State the blood parasite species.
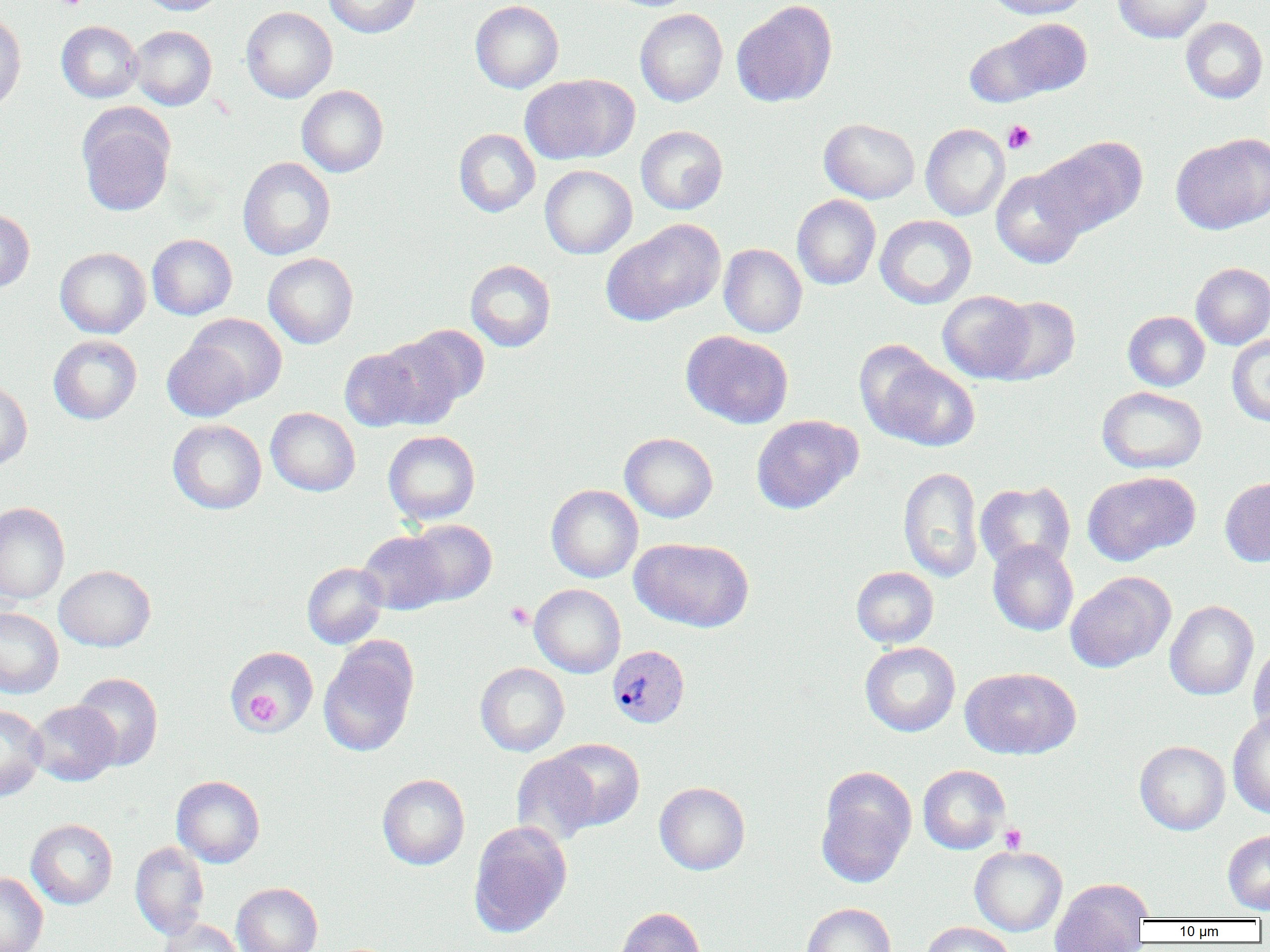
Plasmodium vivax.

Summary:
  - Coordinate format: approximate bounding boxes as [x1, y1, x2, y2] in pixels
  - Plasmodium vivax-infected red blood cell locations: [607, 644, 690, 729]
  - Platelet locations: [53, 0, 89, 11], [1002, 120, 1036, 154], [505, 602, 533, 629], [245, 691, 280, 728], [1000, 824, 1027, 853]
  - Uninfected red blood cell locations: [137, 0, 228, 16], [324, 0, 421, 38], [986, 0, 1089, 19], [1112, 0, 1213, 43], [470, 1, 564, 93], [731, 2, 837, 107], [240, 6, 338, 103], [635, 8, 728, 106], [0, 14, 26, 113], [997, 17, 1093, 98], [1181, 17, 1268, 104], [56, 21, 143, 103], [129, 25, 217, 110], [963, 30, 1056, 107], [520, 74, 637, 165], [297, 85, 389, 177], [77, 107, 175, 217], [819, 118, 920, 203], [921, 123, 1010, 221], [636, 125, 728, 214], [453, 128, 540, 217], [1170, 133, 1270, 234], [1036, 137, 1148, 236], [237, 157, 336, 260], [540, 165, 637, 259], [991, 168, 1086, 268], [792, 194, 881, 290], [0, 208, 34, 294], [875, 215, 977, 309], [602, 219, 725, 325], [147, 234, 237, 319], [719, 244, 807, 337], [55, 247, 151, 338], [263, 253, 358, 349], [465, 259, 556, 352], [1191, 262, 1270, 349], [937, 290, 1036, 383], [988, 296, 1080, 384], [1123, 311, 1210, 391], [183, 313, 287, 407], [379, 325, 488, 420], [681, 330, 793, 429], [1227, 334, 1270, 426], [48, 335, 142, 424], [162, 339, 252, 422], [339, 347, 425, 431], [865, 352, 980, 451], [0, 380, 32, 471], [1097, 386, 1207, 473], [266, 407, 360, 496], [751, 414, 863, 514], [168, 419, 266, 514], [383, 430, 480, 525], [620, 432, 718, 523], [898, 466, 983, 582], [1082, 471, 1199, 565], [1219, 477, 1270, 567], [975, 481, 1076, 573], [546, 484, 643, 583], [0, 502, 70, 604], [405, 519, 497, 606], [357, 530, 451, 614], [632, 538, 754, 632], [988, 540, 1078, 636], [302, 562, 388, 649], [54, 565, 156, 651], [851, 566, 939, 648], [1066, 571, 1175, 672], [529, 584, 626, 677], [1165, 600, 1258, 701], [0, 608, 64, 698], [318, 639, 418, 757], [1248, 641, 1270, 738], [860, 642, 961, 736], [226, 645, 319, 734], [475, 662, 569, 756], [960, 666, 1081, 759], [71, 672, 163, 770], [28, 700, 120, 786], [0, 705, 47, 801], [1228, 712, 1270, 818], [548, 738, 644, 830], [1135, 741, 1230, 835], [510, 752, 601, 847], [918, 764, 1010, 854], [816, 768, 917, 887], [377, 774, 470, 870], [171, 775, 265, 867], [654, 782, 750, 875], [26, 819, 118, 909], [469, 820, 572, 938], [1223, 830, 1270, 914], [130, 841, 209, 940], [969, 845, 1067, 936], [0, 872, 48, 952], [1050, 878, 1152, 952], [232, 882, 322, 952], [801, 902, 896, 952], [614, 906, 707, 952], [156, 919, 245, 952], [921, 921, 1016, 952]
  - Magnification: 1000x
  - Preparation: thin blood film
  - Field of view: one of a larger specimen
  - Modality: light microscopy
  - Image size: 1270×952 pixels